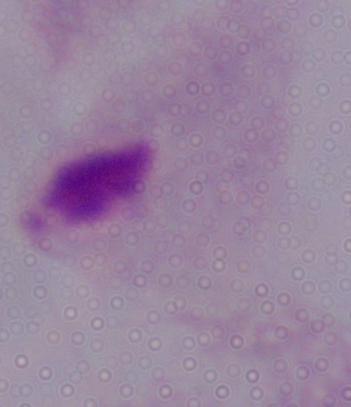

Photomicrograph. 1000x magnification. A trichomonad is seen.